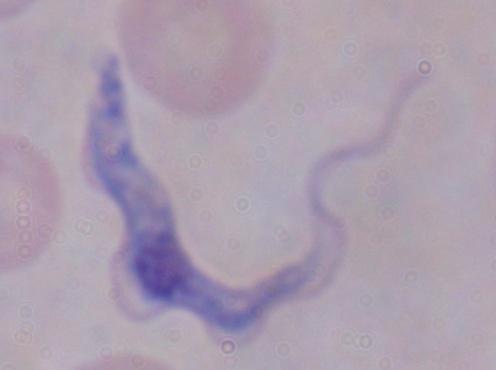 A trypanosome is seen. Micrograph. Captured at 1000x magnification.